Assess the morphology of the red blood cells.
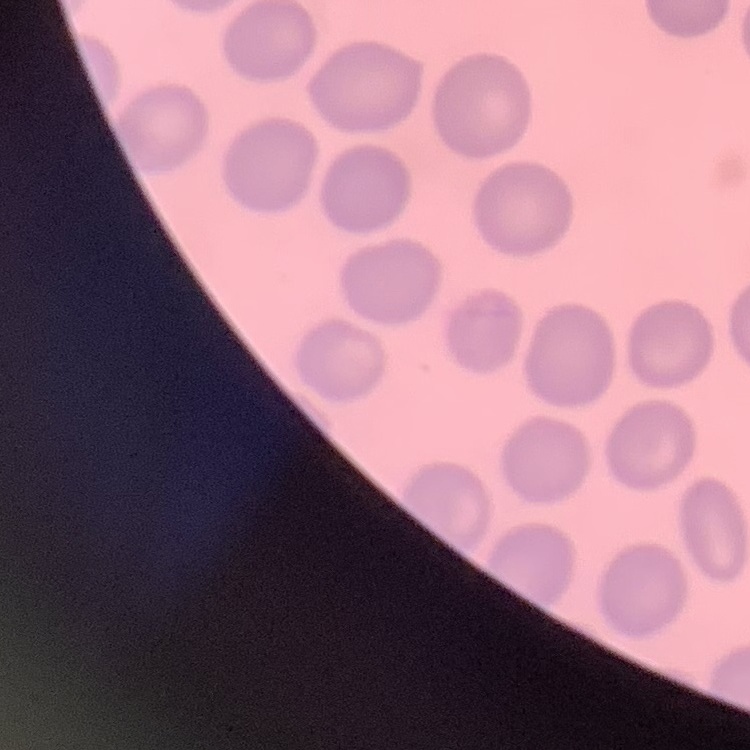

They show no rouleaux formation.

preparation: thin blood smear
stain: Field's or Giemsa
image_type: square crop of a larger photomicrograph